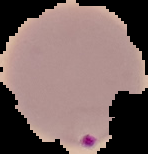

preparation = thin blood film
image type = cell region segmented out of the field of view; surrounding area masked to black
result = Plasmodium parasites identified
image size = 148×154 pixels